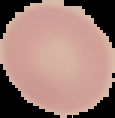 Malaria status: uninfected. From a thin blood film. Segmented cell region on a black background. Image is 115×118 pixels.